Report the malaria status of this cell.
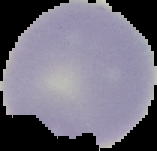
Uninfected.

Summary:
  - Image size: 157×151 pixels
  - Image type: cell region segmented out of the field of view; surrounding area masked to black
  - Preparation: thin blood film